Report the malaria status of this cell.
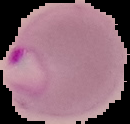

Parasitized.

Image is 130×124 pixels. From a thin blood smear. The area outside the segmented cell region is set to black.